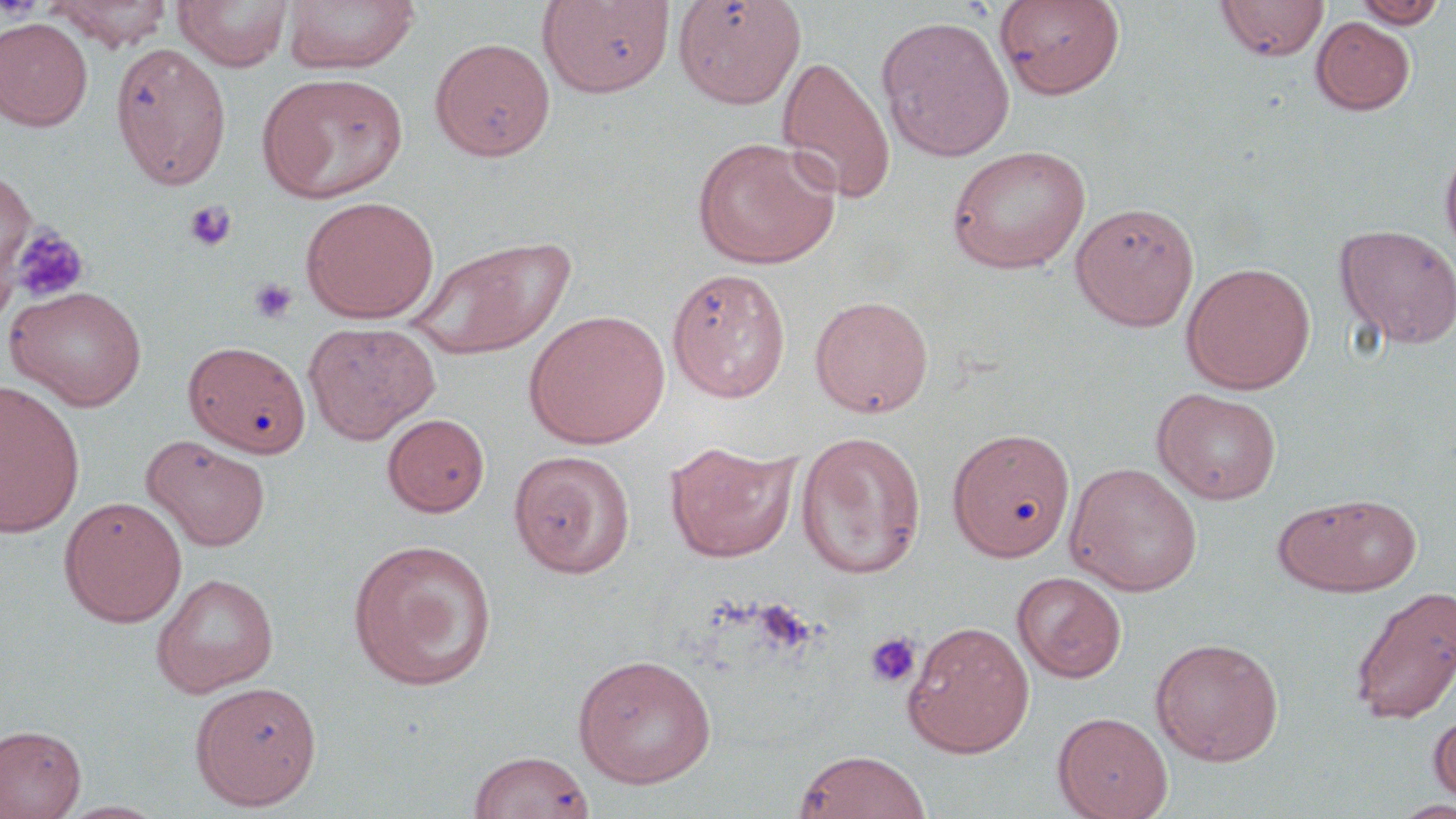
Summary:
  - Coordinate format: approximate bounding boxes as (x1, y1, x2, y2) in pixels
  - Uninfected red blood cell locations: (44, 0, 174, 50), (174, 0, 294, 70), (281, 0, 420, 74), (536, 0, 675, 98), (673, 0, 807, 109), (994, 0, 1126, 99), (1215, 0, 1329, 62), (1352, 0, 1449, 28), (875, 14, 1016, 161), (1311, 16, 1416, 115), (0, 17, 93, 131), (430, 38, 555, 161), (111, 42, 232, 190), (777, 55, 897, 205), (258, 73, 408, 203), (691, 136, 841, 270), (1439, 141, 1456, 264), (945, 145, 1092, 274), (0, 168, 36, 305), (300, 195, 440, 323), (1070, 201, 1200, 331), (1334, 223, 1456, 350), (406, 233, 577, 360), (1181, 261, 1316, 394), (667, 267, 791, 403), (4, 285, 149, 410), (810, 295, 933, 418), (523, 309, 671, 449), (303, 321, 441, 443), (183, 340, 311, 458), (0, 380, 85, 537), (1152, 387, 1283, 505), (382, 413, 490, 517), (947, 427, 1076, 563), (796, 429, 927, 580), (142, 434, 271, 552), (665, 439, 800, 563), (508, 449, 636, 578), (1065, 461, 1203, 596), (1274, 492, 1422, 597), (58, 495, 187, 626), (347, 537, 499, 691), (1012, 571, 1127, 683), (152, 572, 278, 696), (1349, 585, 1456, 725), (902, 620, 1035, 758), (1150, 637, 1284, 765), (572, 653, 717, 788), (189, 680, 322, 810), (1427, 710, 1456, 807), (1052, 711, 1173, 819), (0, 724, 86, 818), (793, 749, 932, 819), (467, 750, 595, 819), (1390, 798, 1455, 818), (56, 799, 170, 818)
  - Platelet locations: (183, 200, 237, 252), (6, 223, 90, 305), (249, 278, 299, 325), (864, 632, 922, 689)
  - Slide-level diagnosis: no evidence of blood parasites
  - Modality: optical microscopy
  - Image size: 1456×819 pixels
  - Magnification: 1000x
  - Stain: May-Grünwald-Giemsa
  - Field of view: one of a larger specimen
  - Preparation: thin blood film